Assess this cell for malaria.
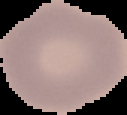
Uninfected.

From a thin blood film. Image is 127×115 pixels. The area outside the segmented cell region is set to black.